Locate and identify every blood parasite.
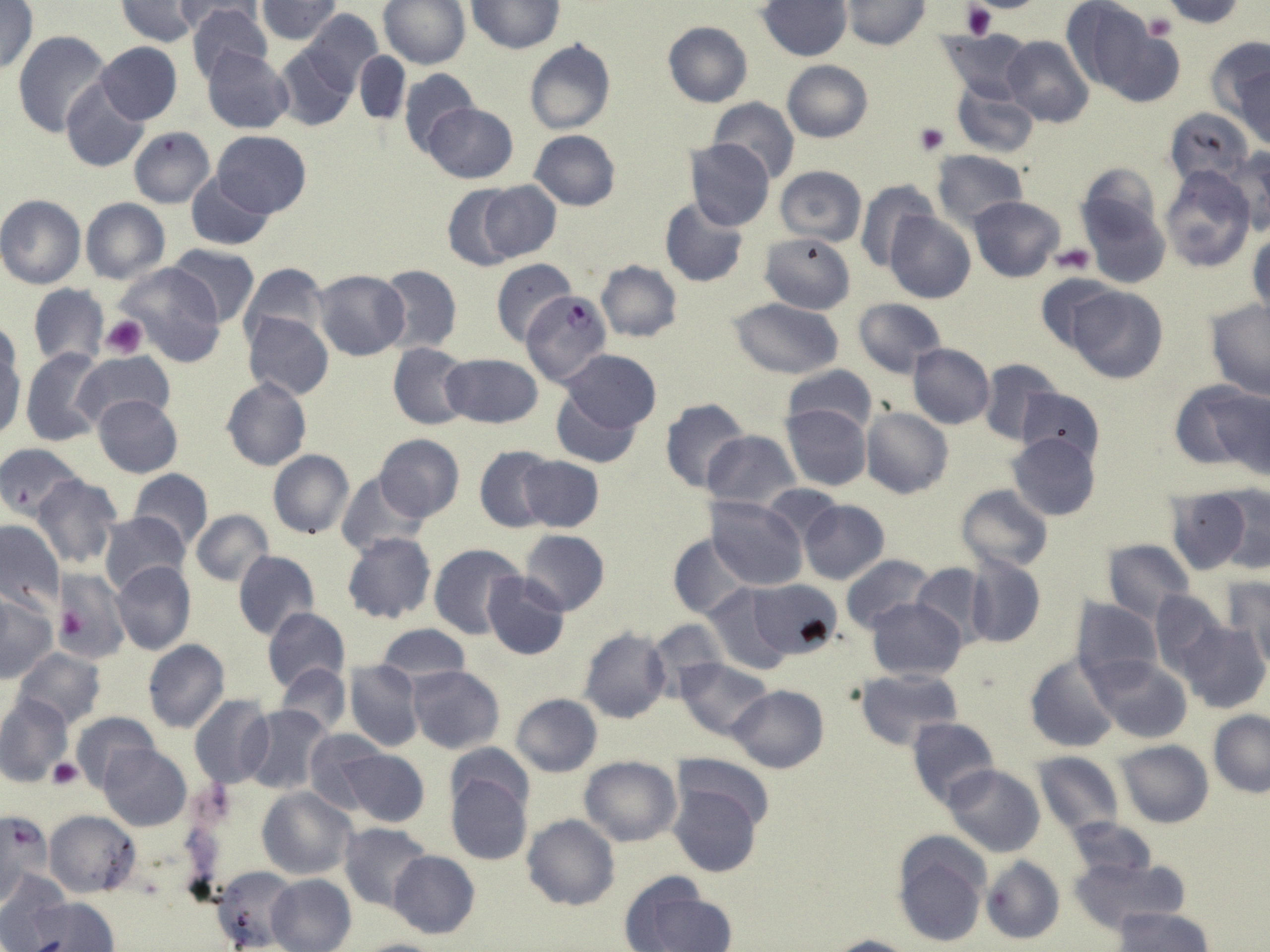
Approximate bounding boxes as named x1/y1/x2/y2 corners in pixels.
Plasmodium falciparum-infected red blood cells: (x1=518, y1=288, x2=611, y2=388).
No Plasmodium ovale, Plasmodium malariae, Plasmodium vivax, Babesia divergens, or Trypanosoma brucei observed.

Summary:
  - Uninfected red blood cell locations: (x1=115, y1=0, x2=204, y2=45), (x1=171, y1=0, x2=265, y2=38), (x1=1059, y1=0, x2=1152, y2=90), (x1=1159, y1=0, x2=1245, y2=26), (x1=0, y1=1, x2=38, y2=75), (x1=256, y1=1, x2=342, y2=42), (x1=379, y1=1, x2=470, y2=68), (x1=469, y1=1, x2=563, y2=52), (x1=759, y1=1, x2=851, y2=60), (x1=842, y1=1, x2=927, y2=50), (x1=186, y1=3, x2=273, y2=85), (x1=300, y1=11, x2=382, y2=91), (x1=663, y1=21, x2=752, y2=108), (x1=1102, y1=27, x2=1185, y2=107), (x1=939, y1=28, x2=1031, y2=103), (x1=13, y1=30, x2=113, y2=138), (x1=1204, y1=34, x2=1270, y2=121), (x1=1001, y1=35, x2=1094, y2=126), (x1=525, y1=40, x2=616, y2=135), (x1=94, y1=43, x2=182, y2=125), (x1=273, y1=45, x2=358, y2=131), (x1=201, y1=46, x2=293, y2=134), (x1=353, y1=50, x2=409, y2=127), (x1=1234, y1=56, x2=1269, y2=150), (x1=782, y1=60, x2=872, y2=143), (x1=398, y1=69, x2=480, y2=156), (x1=61, y1=79, x2=150, y2=172), (x1=952, y1=83, x2=1040, y2=157), (x1=709, y1=98, x2=799, y2=184), (x1=423, y1=103, x2=518, y2=183), (x1=1165, y1=107, x2=1255, y2=190), (x1=128, y1=127, x2=214, y2=208), (x1=530, y1=130, x2=621, y2=211), (x1=212, y1=131, x2=310, y2=217), (x1=687, y1=139, x2=776, y2=233), (x1=1224, y1=147, x2=1270, y2=235), (x1=931, y1=149, x2=1028, y2=229), (x1=1077, y1=163, x2=1162, y2=241), (x1=1159, y1=165, x2=1257, y2=272), (x1=774, y1=166, x2=867, y2=246), (x1=187, y1=173, x2=275, y2=250), (x1=855, y1=179, x2=937, y2=271), (x1=476, y1=181, x2=560, y2=262), (x1=442, y1=184, x2=522, y2=270), (x1=0, y1=195, x2=86, y2=289), (x1=1081, y1=195, x2=1170, y2=288), (x1=969, y1=196, x2=1064, y2=281), (x1=661, y1=197, x2=748, y2=287), (x1=81, y1=198, x2=170, y2=284), (x1=885, y1=212, x2=976, y2=304), (x1=760, y1=231, x2=854, y2=314), (x1=1248, y1=232, x2=1269, y2=319), (x1=166, y1=244, x2=259, y2=327), (x1=490, y1=258, x2=576, y2=345), (x1=595, y1=260, x2=682, y2=342), (x1=238, y1=261, x2=329, y2=350), (x1=112, y1=262, x2=228, y2=366), (x1=376, y1=264, x2=463, y2=352), (x1=311, y1=269, x2=410, y2=360), (x1=1036, y1=274, x2=1121, y2=353), (x1=28, y1=284, x2=108, y2=369), (x1=1066, y1=287, x2=1168, y2=383), (x1=853, y1=296, x2=947, y2=378), (x1=726, y1=298, x2=846, y2=379), (x1=1203, y1=300, x2=1270, y2=399), (x1=244, y1=312, x2=334, y2=400), (x1=0, y1=334, x2=25, y2=437), (x1=387, y1=342, x2=472, y2=430), (x1=907, y1=343, x2=996, y2=428), (x1=21, y1=348, x2=105, y2=445), (x1=555, y1=349, x2=662, y2=438), (x1=71, y1=352, x2=175, y2=433), (x1=442, y1=354, x2=543, y2=429), (x1=977, y1=356, x2=1063, y2=446), (x1=782, y1=364, x2=878, y2=436), (x1=221, y1=376, x2=311, y2=471), (x1=547, y1=378, x2=649, y2=470), (x1=1174, y1=383, x2=1265, y2=476), (x1=1016, y1=387, x2=1105, y2=467), (x1=93, y1=396, x2=182, y2=477), (x1=659, y1=398, x2=750, y2=495), (x1=782, y1=404, x2=872, y2=491), (x1=861, y1=407, x2=953, y2=499), (x1=704, y1=429, x2=799, y2=512), (x1=1006, y1=432, x2=1102, y2=523), (x1=374, y1=434, x2=465, y2=522), (x1=0, y1=443, x2=83, y2=521), (x1=474, y1=444, x2=557, y2=532), (x1=268, y1=450, x2=354, y2=539), (x1=517, y1=456, x2=603, y2=533), (x1=129, y1=468, x2=214, y2=548), (x1=337, y1=473, x2=429, y2=558), (x1=32, y1=474, x2=120, y2=570), (x1=956, y1=484, x2=1053, y2=573), (x1=760, y1=485, x2=843, y2=547), (x1=1216, y1=485, x2=1270, y2=574), (x1=1165, y1=489, x2=1252, y2=574), (x1=707, y1=496, x2=808, y2=592), (x1=798, y1=499, x2=889, y2=583), (x1=190, y1=510, x2=274, y2=588), (x1=98, y1=511, x2=189, y2=595), (x1=0, y1=519, x2=65, y2=617), (x1=518, y1=529, x2=610, y2=616), (x1=342, y1=531, x2=436, y2=624), (x1=667, y1=532, x2=750, y2=620), (x1=1101, y1=539, x2=1195, y2=620), (x1=429, y1=543, x2=527, y2=640), (x1=232, y1=549, x2=319, y2=641), (x1=962, y1=552, x2=1046, y2=649), (x1=841, y1=555, x2=936, y2=636), (x1=110, y1=560, x2=197, y2=655), (x1=911, y1=562, x2=992, y2=646), (x1=54, y1=568, x2=130, y2=664), (x1=482, y1=572, x2=571, y2=660), (x1=1221, y1=577, x2=1270, y2=668), (x1=746, y1=578, x2=842, y2=661), (x1=701, y1=582, x2=795, y2=675), (x1=674, y1=588, x2=784, y2=726), (x1=1148, y1=588, x2=1228, y2=679), (x1=0, y1=595, x2=57, y2=682), (x1=1072, y1=596, x2=1162, y2=685), (x1=866, y1=597, x2=967, y2=681), (x1=262, y1=607, x2=349, y2=692), (x1=646, y1=618, x2=728, y2=700), (x1=1175, y1=620, x2=1268, y2=714), (x1=375, y1=624, x2=471, y2=687), (x1=577, y1=627, x2=672, y2=725), (x1=143, y1=640, x2=229, y2=733), (x1=13, y1=647, x2=106, y2=729), (x1=1023, y1=653, x2=1120, y2=753), (x1=1085, y1=655, x2=1194, y2=742), (x1=675, y1=658, x2=773, y2=739), (x1=345, y1=660, x2=423, y2=752), (x1=275, y1=663, x2=351, y2=737), (x1=409, y1=665, x2=504, y2=753), (x1=853, y1=669, x2=963, y2=751), (x1=728, y1=684, x2=829, y2=773), (x1=0, y1=693, x2=73, y2=787), (x1=510, y1=694, x2=603, y2=776), (x1=189, y1=695, x2=273, y2=790), (x1=0, y1=702, x2=152, y2=782), (x1=243, y1=705, x2=334, y2=795), (x1=70, y1=711, x2=160, y2=793), (x1=1208, y1=711, x2=1269, y2=798), (x1=906, y1=715, x2=998, y2=809), (x1=304, y1=727, x2=385, y2=812), (x1=1115, y1=740, x2=1213, y2=828), (x1=446, y1=743, x2=533, y2=818), (x1=101, y1=744, x2=191, y2=831), (x1=336, y1=749, x2=430, y2=828), (x1=1030, y1=752, x2=1124, y2=835), (x1=672, y1=753, x2=776, y2=834), (x1=579, y1=755, x2=680, y2=846), (x1=943, y1=765, x2=1046, y2=857), (x1=444, y1=770, x2=533, y2=867), (x1=669, y1=783, x2=761, y2=877), (x1=258, y1=787, x2=355, y2=880), (x1=44, y1=810, x2=140, y2=898), (x1=0, y1=811, x2=50, y2=905), (x1=521, y1=814, x2=619, y2=911), (x1=1064, y1=817, x2=1157, y2=880), (x1=338, y1=822, x2=432, y2=911), (x1=891, y1=832, x2=991, y2=947), (x1=387, y1=850, x2=479, y2=939), (x1=980, y1=855, x2=1065, y2=945), (x1=1070, y1=855, x2=1188, y2=933), (x1=212, y1=866, x2=299, y2=950), (x1=0, y1=871, x2=70, y2=949), (x1=266, y1=875, x2=356, y2=952), (x1=624, y1=880, x2=737, y2=952), (x1=26, y1=897, x2=119, y2=951), (x1=1111, y1=906, x2=1214, y2=952), (x1=821, y1=934, x2=914, y2=952), (x1=350, y1=938, x2=452, y2=952)
  - Platelet locations: (x1=961, y1=3, x2=997, y2=39), (x1=1144, y1=12, x2=1179, y2=41), (x1=914, y1=123, x2=949, y2=155), (x1=1052, y1=244, x2=1096, y2=275), (x1=102, y1=315, x2=148, y2=358), (x1=48, y1=758, x2=82, y2=790)
  - Slide-level diagnosis: Plasmodium falciparum
  - Image size: 1270×952 pixels
  - Field of view: one of a larger specimen
  - Magnification: 1000x
  - Preparation: thin blood film
  - Modality: optical microscopy
  - Stain: May-Grünwald-Giemsa